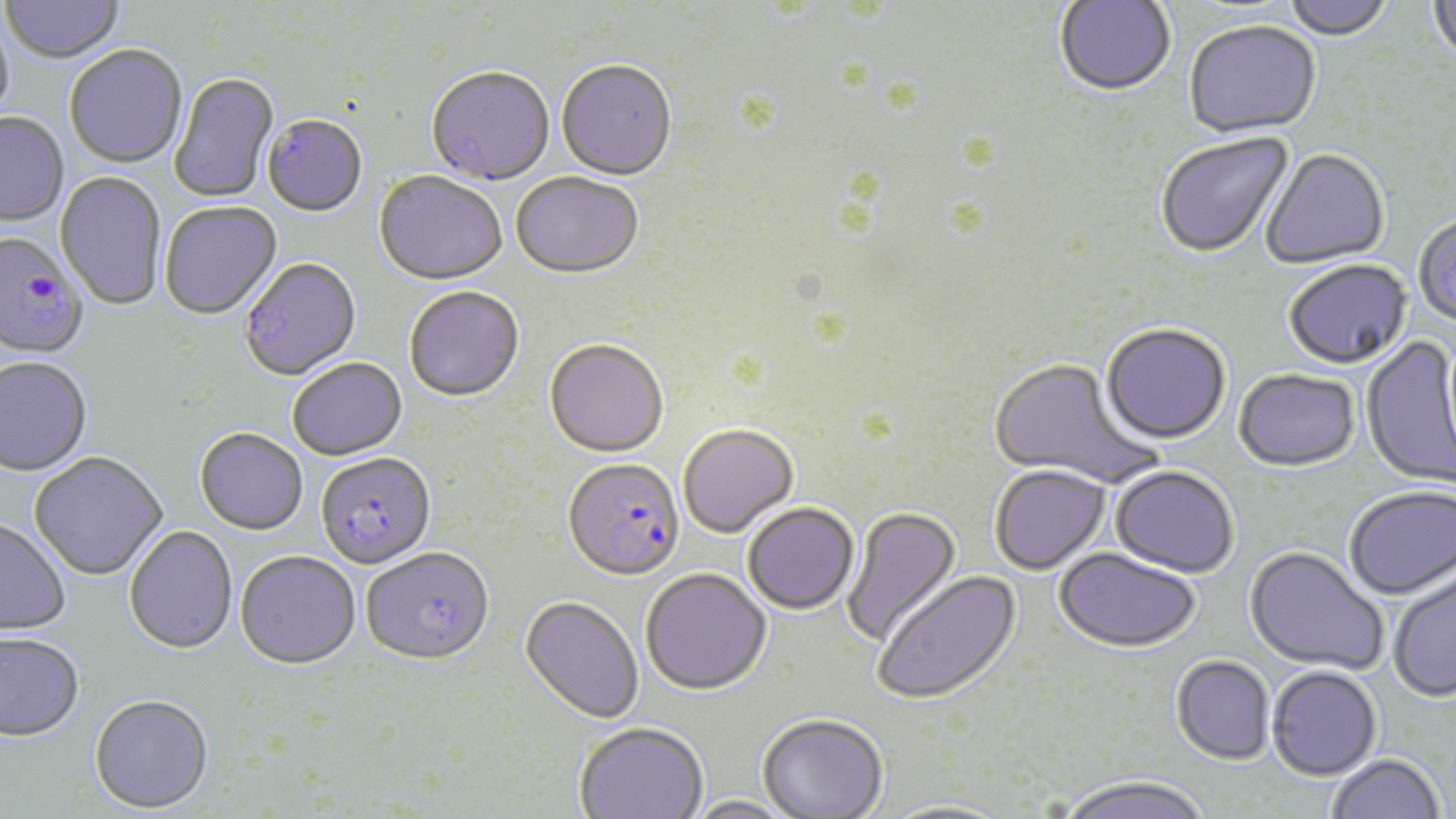 Approximate bounding boxes as (x1,y1)-(x2,y2) corner pairs in pixels. Plasmodium falciparum-infected red blood cell locations: (0,233)-(89,361), (315,453)-(436,570), (562,458)-(685,582). Uninfected red blood cell locations: (1055,0)-(1176,99), (1280,0)-(1395,43), (1427,0)-(1456,72), (1,1)-(125,65), (0,11)-(16,131), (1183,23)-(1321,140), (65,47)-(187,169), (556,63)-(677,183), (426,68)-(554,187), (170,73)-(279,204), (0,113)-(69,227), (262,116)-(368,218), (1155,133)-(1294,260), (1260,149)-(1390,271), (55,171)-(166,312), (373,173)-(508,288), (511,174)-(643,281), (159,202)-(282,320), (1413,215)-(1456,329), (240,258)-(362,382), (1283,261)-(1412,371), (404,288)-(525,403), (1100,325)-(1230,446), (1361,335)-(1456,490), (544,341)-(669,459), (0,358)-(93,477), (989,358)-(1161,489), (288,359)-(407,461), (1234,369)-(1361,474), (678,425)-(799,539), (194,429)-(308,536), (29,452)-(167,581), (989,466)-(1111,575), (1110,466)-(1239,578), (1344,486)-(1456,601), (743,503)-(860,615), (842,506)-(962,648), (0,519)-(71,637), (124,526)-(238,655), (1244,546)-(1388,674), (362,547)-(495,667), (1054,547)-(1201,653), (235,552)-(360,671), (640,569)-(771,696), (1387,569)-(1456,703), (872,571)-(1022,706), (520,596)-(644,724), (0,633)-(85,741), (1171,655)-(1275,765), (1266,666)-(1382,780), (89,694)-(213,813), (757,714)-(889,818), (574,722)-(708,819), (1325,753)-(1446,819), (1054,777)-(1213,819), (684,796)-(799,819), (878,799)-(1016,819). Slide-level diagnosis: Plasmodium falciparum. Optical microscopy. 1000x magnification. Single field of view. Image is 1456×819 pixels. Thin blood film. May-Grünwald-Giemsa stain.